Assess this cell for malaria.
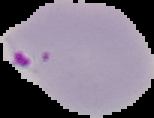

Parasitized.

Summary:
  - Image type: segmented cell region on a black background
  - Preparation: thin blood film
  - Image size: 154×118 pixels